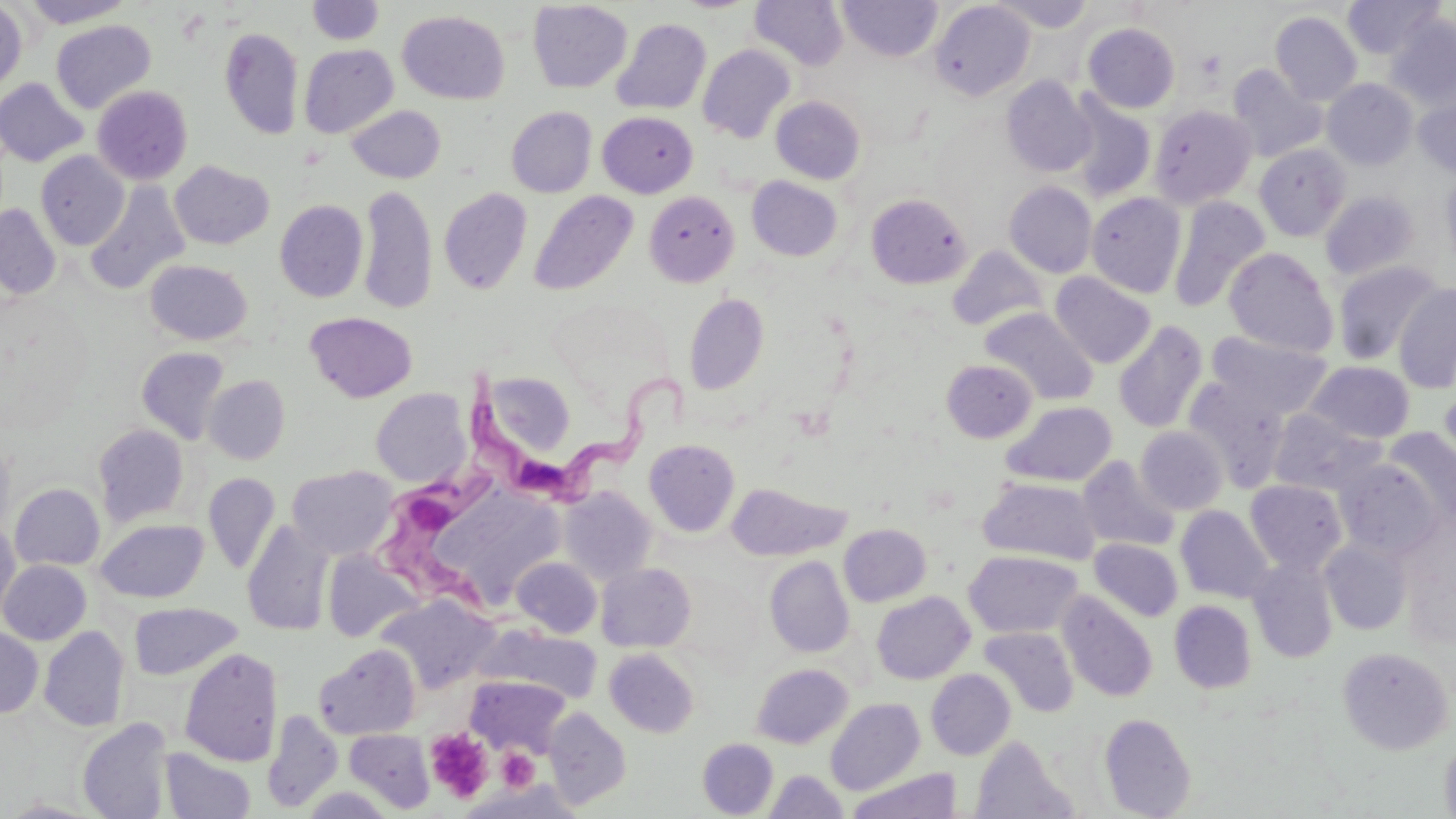

slide-level diagnosis = Trypanosoma brucei
uninfected red blood cell locations = approximate bounding boxes as [x1, y1, x2, y2] in pixels: [20, 0, 134, 27], [839, 0, 942, 62], [991, 0, 1095, 32], [1343, 0, 1443, 60], [0, 1, 28, 95], [306, 1, 385, 45], [528, 1, 632, 93], [749, 1, 849, 70], [929, 1, 1034, 100], [397, 10, 509, 104], [1270, 11, 1361, 105], [1386, 14, 1456, 112], [611, 18, 711, 115], [51, 19, 156, 114], [1083, 23, 1180, 112], [219, 26, 304, 139], [299, 44, 398, 138], [697, 44, 796, 143], [1227, 64, 1328, 162], [1001, 76, 1097, 177], [0, 77, 89, 167], [1322, 79, 1418, 169], [92, 85, 193, 185], [1413, 92, 1456, 179], [1064, 94, 1157, 202], [771, 96, 866, 185], [1150, 104, 1257, 206], [346, 105, 446, 183], [506, 106, 597, 197], [598, 111, 698, 198], [1254, 144, 1351, 241], [36, 151, 130, 250], [169, 160, 274, 249], [1441, 171, 1456, 275], [746, 176, 843, 261], [84, 180, 190, 295], [1004, 182, 1097, 277], [358, 184, 437, 315], [438, 188, 533, 294], [529, 190, 638, 296], [644, 190, 740, 287], [1320, 191, 1419, 280], [1086, 192, 1187, 298], [865, 193, 971, 289], [1169, 196, 1270, 312], [275, 199, 368, 302], [0, 204, 61, 299], [947, 246, 1048, 332], [1223, 247, 1338, 357], [145, 260, 253, 345], [1331, 260, 1444, 365], [1050, 272, 1156, 368], [1394, 283, 1456, 393], [684, 292, 768, 395], [980, 307, 1097, 405], [305, 312, 417, 402], [1113, 321, 1208, 434], [1206, 331, 1332, 419], [136, 347, 230, 445], [942, 359, 1037, 442], [1305, 360, 1415, 443], [483, 371, 576, 458], [205, 375, 290, 463], [1184, 378, 1290, 491], [1438, 385, 1456, 486], [371, 388, 470, 487], [1002, 401, 1117, 487], [1268, 409, 1385, 496], [93, 424, 190, 526], [1136, 426, 1228, 515], [1382, 428, 1455, 526], [644, 439, 739, 536], [1077, 456, 1180, 553], [1336, 459, 1442, 559], [287, 465, 398, 560], [203, 472, 280, 574], [978, 477, 1100, 565], [1245, 479, 1348, 574], [726, 482, 850, 561], [11, 483, 105, 570], [420, 486, 567, 611], [560, 486, 658, 583], [1176, 505, 1275, 603], [96, 518, 208, 603], [0, 520, 20, 623], [241, 521, 335, 637], [839, 523, 931, 606], [1320, 538, 1413, 635], [1090, 539, 1183, 621], [323, 550, 423, 643], [964, 550, 1082, 638], [765, 556, 854, 657], [512, 557, 602, 638], [1246, 558, 1339, 662], [1, 560, 91, 645], [596, 563, 696, 652], [872, 591, 975, 684], [1058, 591, 1158, 702], [377, 595, 498, 694], [1169, 600, 1257, 693], [129, 603, 243, 680], [39, 626, 130, 732], [979, 626, 1079, 718], [0, 627, 43, 717], [484, 627, 601, 704], [313, 644, 421, 739], [1336, 646, 1453, 755], [180, 648, 283, 766], [604, 649, 700, 737], [751, 663, 853, 748], [926, 669, 1016, 760], [466, 675, 569, 756], [826, 698, 925, 795], [544, 708, 632, 810], [263, 710, 342, 813], [1099, 712, 1196, 818], [77, 717, 174, 818], [263, 717, 436, 812], [345, 730, 435, 813], [1439, 734, 1456, 819], [971, 735, 1076, 819], [697, 738, 778, 817], [160, 748, 256, 819], [847, 768, 962, 818], [764, 770, 847, 818], [459, 780, 586, 819]
platelet locations = approximate bounding boxes as [x1, y1, x2, y2] in pixels: [424, 728, 493, 802], [497, 748, 539, 790]
Trypanosoma brucei locations = approximate bounding boxes as [x1, y1, x2, y2] in pixels: [472, 353, 697, 513], [373, 434, 513, 628]
magnification = 1000x
image size = 1456×819 pixels
modality = light microscopy
field of view = one of a larger specimen
stain = May-Grünwald-Giemsa
preparation = thin blood smear